Name the blood parasite species.
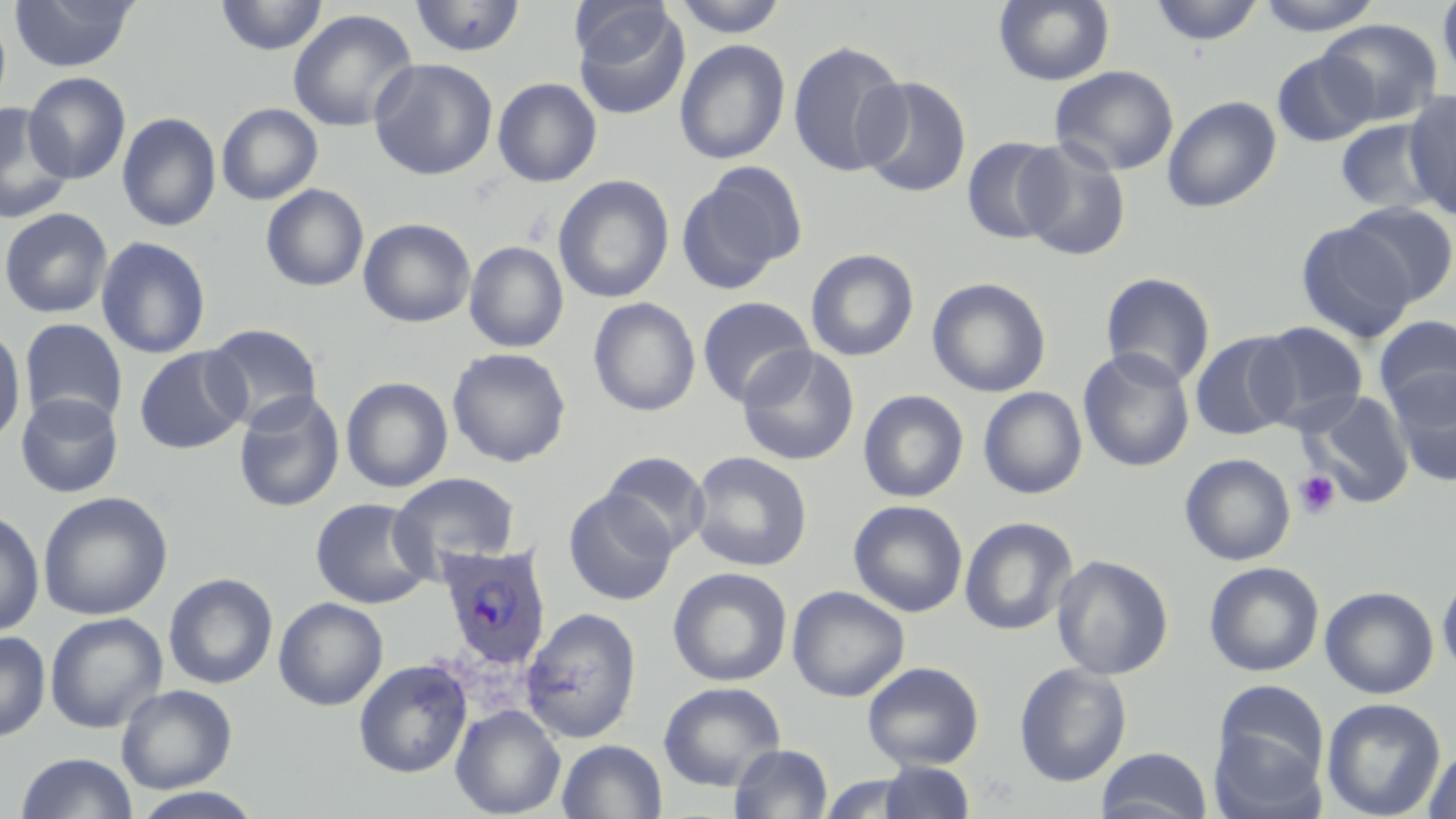

Plasmodium ovale.

Approximate bounding boxes as (x1, y1, x2, y2) in pixels. Plasmodium ovale-infected red blood cell locations: (436, 543, 552, 670). Uninfected red blood cell locations: (8, 0, 138, 73), (215, 0, 328, 56), (409, 0, 526, 58), (670, 0, 789, 37), (994, 0, 1114, 86), (1148, 0, 1265, 46), (1255, 0, 1385, 36), (1438, 0, 1456, 86), (570, 1, 675, 67), (573, 5, 690, 121), (0, 6, 12, 116), (287, 9, 418, 132), (1319, 18, 1443, 125), (577, 19, 767, 144), (674, 39, 790, 164), (787, 39, 909, 178), (1272, 49, 1378, 147), (369, 58, 498, 180), (1050, 65, 1179, 176), (23, 71, 131, 184), (856, 76, 972, 198), (492, 77, 602, 187), (1402, 89, 1456, 219), (1162, 95, 1282, 213), (0, 102, 74, 225), (216, 102, 323, 205), (117, 112, 221, 232), (112, 114, 217, 359), (1335, 118, 1443, 215), (961, 136, 1066, 244), (1015, 138, 1132, 261), (677, 163, 806, 293), (553, 174, 674, 304), (260, 183, 369, 292), (1342, 200, 1456, 305), (0, 208, 112, 318), (358, 217, 475, 327), (1297, 221, 1417, 342), (95, 236, 211, 359), (464, 241, 568, 353), (805, 248, 919, 362), (1100, 272, 1217, 390), (927, 277, 1051, 397), (697, 296, 815, 407), (587, 297, 701, 417), (1374, 316, 1456, 418), (19, 319, 127, 428), (1251, 322, 1369, 432), (203, 323, 324, 430), (0, 324, 27, 448), (1190, 331, 1299, 441), (737, 344, 859, 465), (134, 346, 249, 454), (447, 347, 572, 468), (1078, 348, 1195, 472), (1388, 369, 1456, 485), (340, 377, 453, 493), (978, 386, 1088, 499), (858, 389, 969, 503), (233, 390, 345, 512), (1301, 391, 1415, 507), (15, 392, 123, 498), (600, 451, 710, 554), (688, 451, 813, 572), (1179, 453, 1295, 566), (390, 471, 521, 574), (563, 489, 678, 606), (37, 491, 173, 620), (310, 497, 434, 609), (848, 499, 968, 617), (0, 510, 45, 638), (959, 516, 1078, 636), (1051, 554, 1174, 680), (1203, 561, 1324, 677), (668, 567, 793, 687), (1437, 569, 1456, 680), (163, 573, 278, 689), (786, 585, 910, 702), (1320, 586, 1439, 699), (273, 597, 389, 711), (520, 607, 642, 743), (45, 612, 167, 733), (0, 631, 51, 742), (353, 659, 472, 778), (862, 661, 984, 769), (1014, 662, 1131, 787), (1213, 680, 1329, 784), (658, 681, 786, 791), (116, 684, 237, 793), (1321, 697, 1446, 819), (450, 704, 566, 818), (1210, 725, 1326, 819), (557, 739, 667, 819), (729, 744, 833, 819), (1422, 746, 1456, 819), (1096, 747, 1213, 819), (15, 752, 138, 819), (876, 761, 978, 819), (815, 773, 925, 818), (129, 787, 266, 819). Platelet locations: (1293, 469, 1341, 519). Image is 1456×819 pixels. Single field of view. Optical microscopy. May-Grünwald-Giemsa-stained preparation. Thin blood film. 1000x magnification.